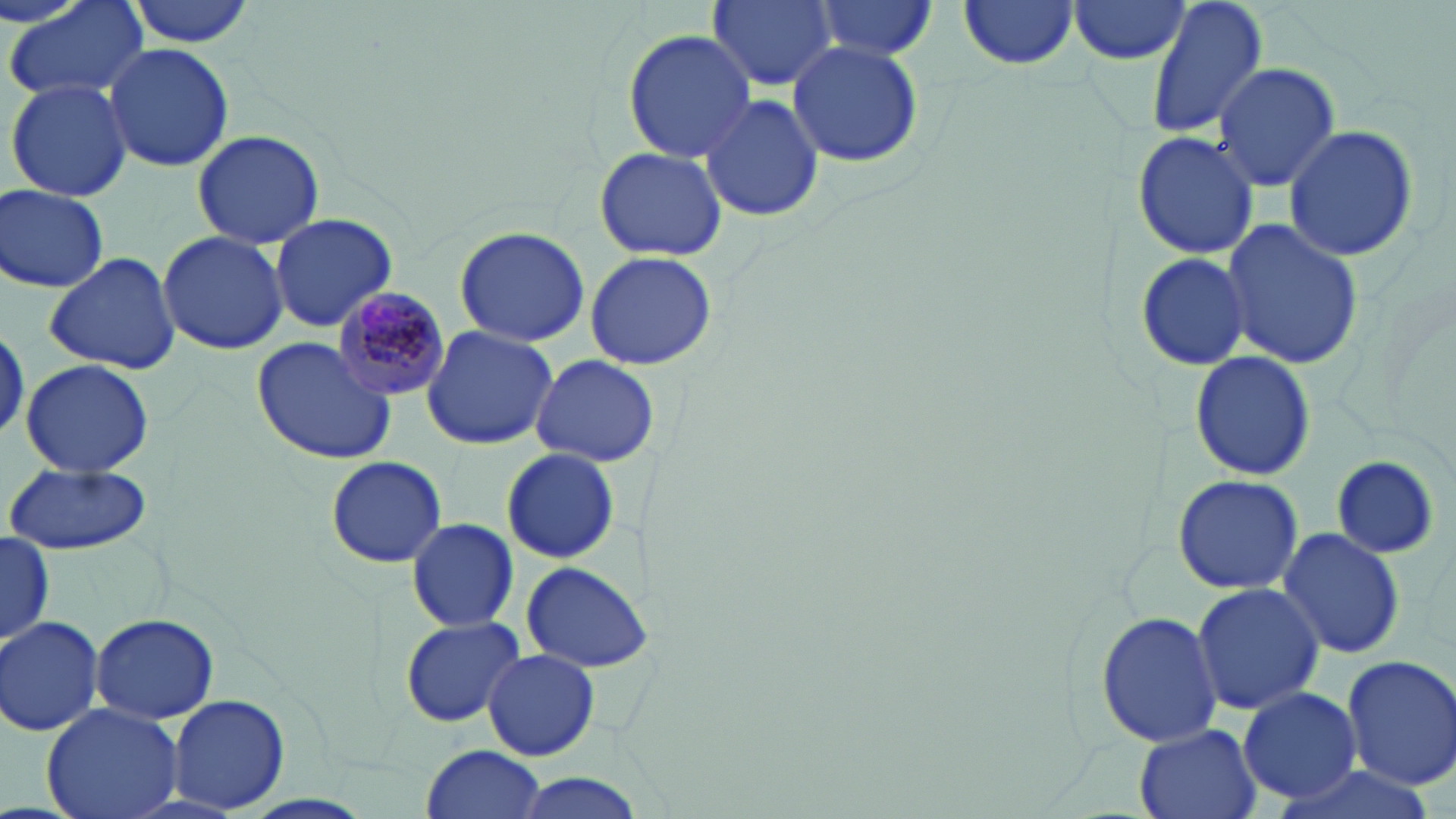

{
  "plasmodium_malariae_infected_red_blood_cell_locations": "approximate bounding boxes as named x1/y1/x2/y2 corners in pixels: (x1=331, y1=287, x2=453, y2=402)",
  "slide_level_diagnosis": "Plasmodium malariae",
  "field_of_view": "one of a larger specimen",
  "image_size": "1456×819 pixels",
  "stain": "May-Grünwald-Giemsa",
  "modality": "light microscopy",
  "magnification": "1000x",
  "preparation": "thin blood smear",
  "uninfected_red_blood_cell_locations": "approximate bounding boxes as named x1/y1/x2/y2 corners in pixels: (x1=6, y1=0, x2=149, y2=105), (x1=126, y1=0, x2=259, y2=47), (x1=708, y1=0, x2=837, y2=90), (x1=1067, y1=0, x2=1194, y2=65), (x1=1142, y1=0, x2=1270, y2=142), (x1=957, y1=1, x2=1081, y2=71), (x1=810, y1=2, x2=939, y2=60), (x1=624, y1=28, x2=755, y2=162), (x1=789, y1=42, x2=923, y2=168), (x1=104, y1=43, x2=235, y2=174), (x1=1211, y1=63, x2=1341, y2=191), (x1=6, y1=78, x2=134, y2=202), (x1=697, y1=94, x2=823, y2=222), (x1=1283, y1=123, x2=1421, y2=261), (x1=190, y1=129, x2=330, y2=250), (x1=1131, y1=130, x2=1260, y2=260), (x1=593, y1=145, x2=728, y2=263), (x1=1, y1=183, x2=111, y2=295), (x1=268, y1=213, x2=399, y2=333), (x1=1220, y1=218, x2=1364, y2=370), (x1=452, y1=225, x2=591, y2=348), (x1=157, y1=231, x2=290, y2=355), (x1=585, y1=249, x2=717, y2=371), (x1=1134, y1=249, x2=1252, y2=374), (x1=44, y1=251, x2=184, y2=376), (x1=422, y1=325, x2=557, y2=450), (x1=251, y1=336, x2=397, y2=464), (x1=1189, y1=352, x2=1315, y2=482), (x1=528, y1=355, x2=659, y2=467), (x1=21, y1=358, x2=156, y2=477), (x1=502, y1=448, x2=620, y2=563), (x1=1331, y1=455, x2=1440, y2=559), (x1=325, y1=456, x2=446, y2=568), (x1=5, y1=462, x2=152, y2=555), (x1=1173, y1=472, x2=1303, y2=595), (x1=406, y1=518, x2=518, y2=633), (x1=1276, y1=529, x2=1404, y2=660), (x1=0, y1=532, x2=56, y2=646), (x1=522, y1=562, x2=651, y2=672), (x1=1192, y1=581, x2=1323, y2=716), (x1=1096, y1=608, x2=1223, y2=748), (x1=90, y1=614, x2=219, y2=723), (x1=0, y1=615, x2=105, y2=736), (x1=400, y1=615, x2=527, y2=728), (x1=483, y1=649, x2=599, y2=761), (x1=1340, y1=653, x2=1456, y2=792), (x1=1238, y1=686, x2=1363, y2=805), (x1=168, y1=693, x2=288, y2=813), (x1=41, y1=701, x2=185, y2=819), (x1=1135, y1=726, x2=1256, y2=819), (x1=422, y1=743, x2=544, y2=817), (x1=503, y1=773, x2=652, y2=819)"
}